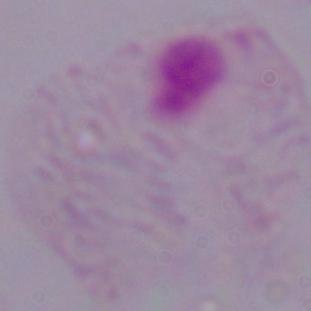

modality = micrograph
magnification = 1000x
identification = trichomonad